Assess this cell for malaria.
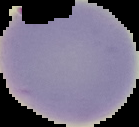
Uninfected.

Summary:
  - Image size: 139×127 pixels
  - Preparation: thin blood film
  - Image type: segmented cell region with the area outside set to black